Identify the blood parasite species.
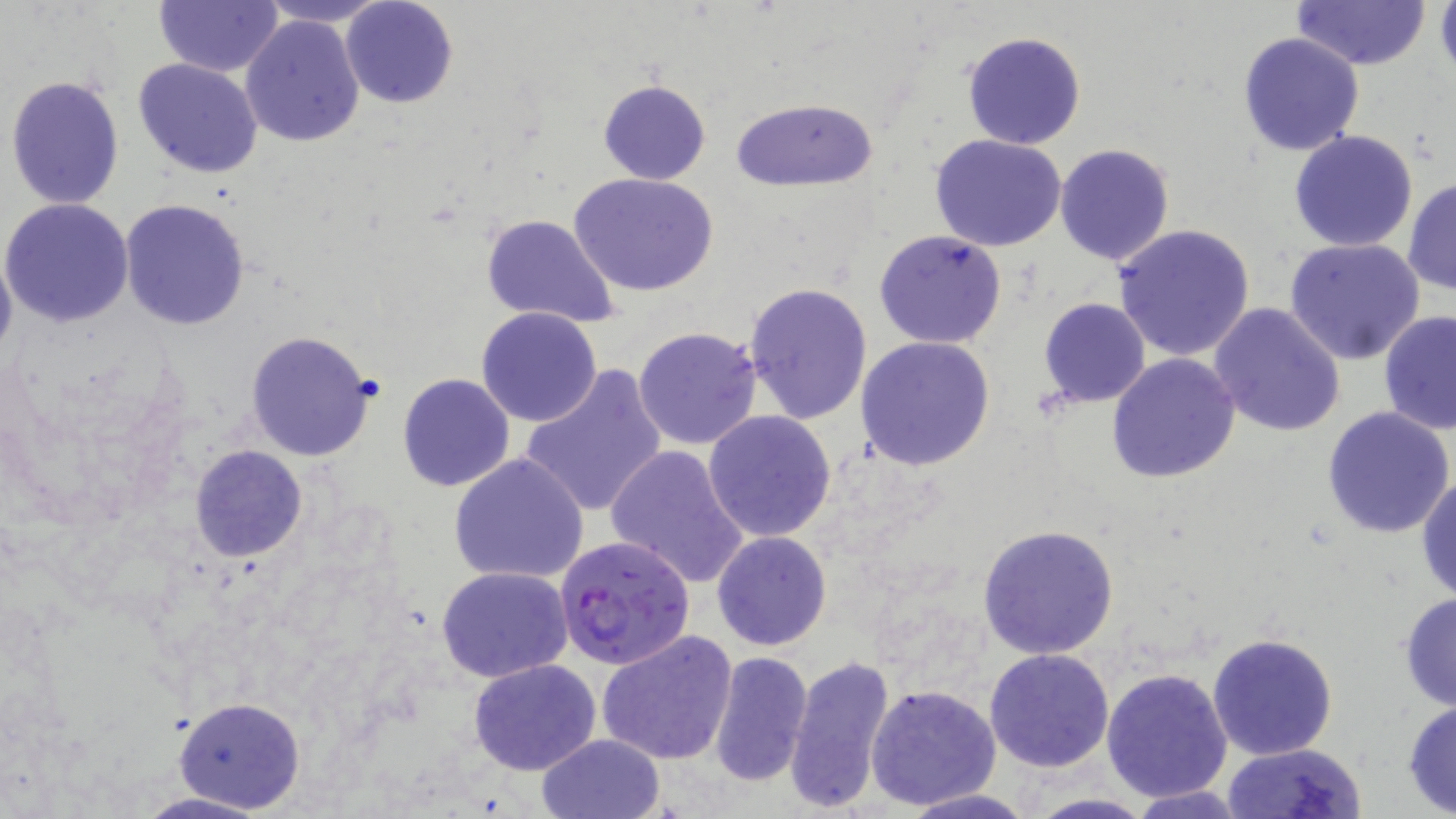

Plasmodium falciparum.

Summary:
  - Coordinate format: approximate bounding boxes as [x1, y1, x2, y2] in pixels
  - Uninfected red blood cell locations: [255, 0, 391, 27], [1292, 0, 1431, 71], [1434, 0, 1456, 84], [154, 1, 283, 75], [339, 1, 459, 109], [240, 14, 367, 147], [961, 30, 1087, 151], [1237, 31, 1365, 157], [133, 57, 262, 177], [5, 74, 125, 210], [597, 79, 711, 185], [730, 96, 878, 192], [1289, 129, 1419, 252], [929, 133, 1068, 251], [1054, 144, 1175, 267], [570, 172, 718, 297], [1404, 177, 1456, 295], [1, 197, 134, 327], [118, 197, 251, 331], [479, 213, 623, 330], [1113, 223, 1258, 362], [874, 229, 1008, 349], [1283, 238, 1427, 366], [0, 244, 16, 368], [744, 281, 872, 424], [1038, 298, 1151, 408], [1207, 301, 1348, 437], [637, 306, 868, 438], [475, 307, 603, 427], [1380, 310, 1456, 435], [632, 326, 763, 449], [246, 330, 379, 462], [856, 336, 995, 470], [1106, 352, 1241, 483], [519, 365, 669, 518], [397, 373, 517, 492], [1322, 406, 1455, 539], [702, 409, 838, 542], [605, 444, 750, 589], [189, 445, 309, 562], [448, 453, 591, 585], [1416, 475, 1456, 601], [975, 523, 1120, 660], [712, 530, 832, 650], [436, 566, 574, 682], [1397, 592, 1456, 711], [595, 627, 739, 764], [1206, 632, 1339, 760], [984, 648, 1115, 772], [1114, 649, 1346, 789], [706, 650, 812, 787], [783, 653, 896, 814], [467, 657, 602, 775], [871, 663, 1115, 790], [1101, 667, 1232, 803], [867, 682, 1000, 810], [175, 698, 306, 812], [1401, 699, 1456, 817], [537, 733, 665, 818], [1222, 742, 1366, 819], [1126, 785, 1252, 818], [898, 788, 1037, 819], [126, 790, 277, 819], [1018, 794, 1160, 819]
  - Plasmodium falciparum-infected red blood cell locations: [555, 533, 696, 670]
  - Field of view: one of a larger specimen
  - Magnification: 1000x
  - Image size: 1456×819 pixels
  - Stain: May-Grünwald-Giemsa
  - Modality: optical microscopy
  - Preparation: thin blood film